Assess for malaria.
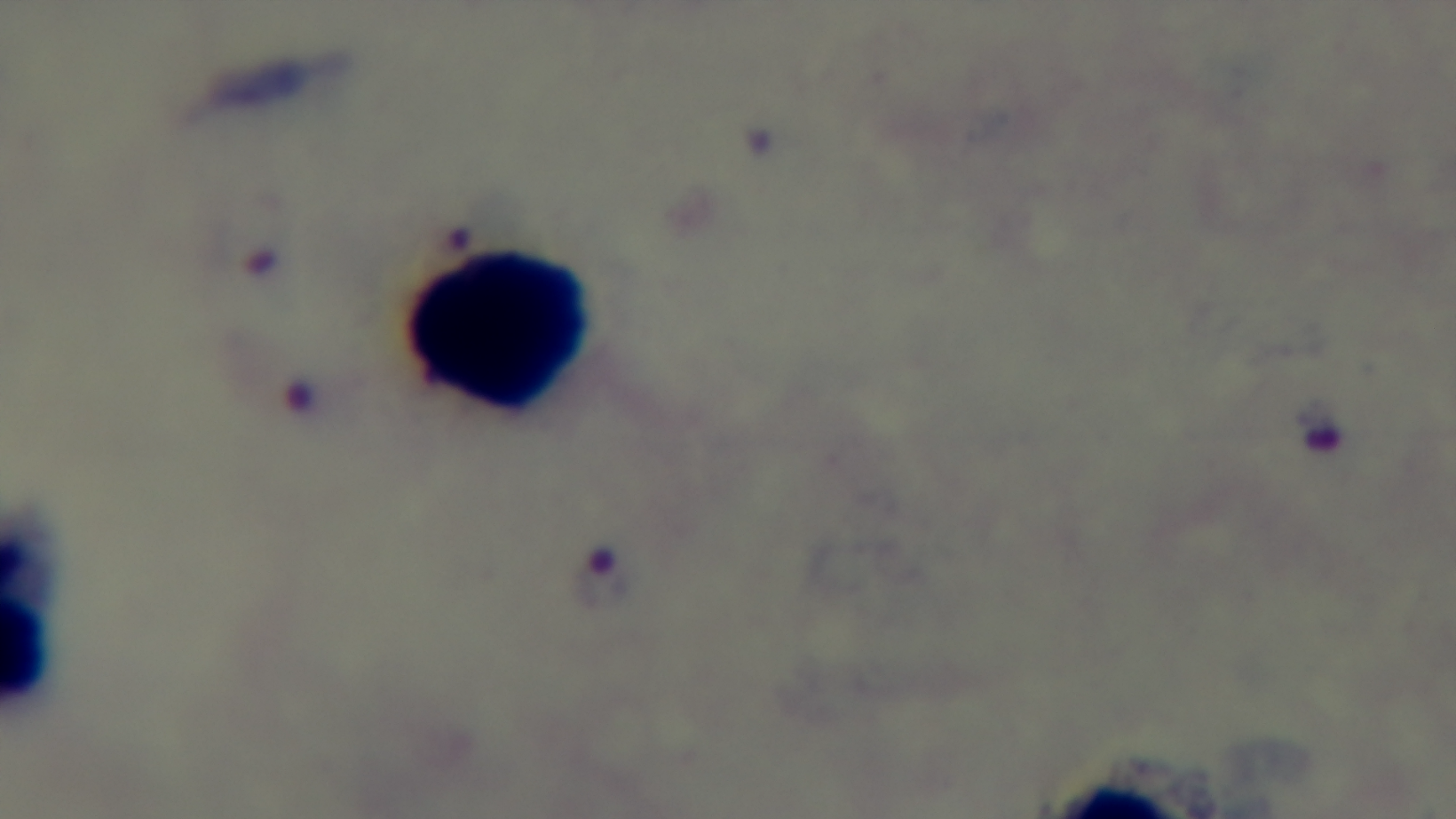
It is infected.

Photomicrograph. Mounted 4K digital camera. Single field of view. Preparation: thick blood film. Oil-immersion objective, 100x. Giemsa stain.